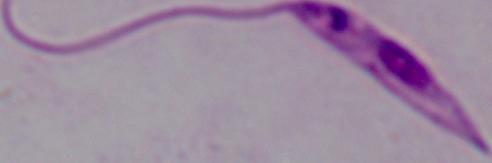

A Leishmania parasite is shown. Micrograph. Captured at 1000x magnification.